Locate every blood parasite and identify its species.
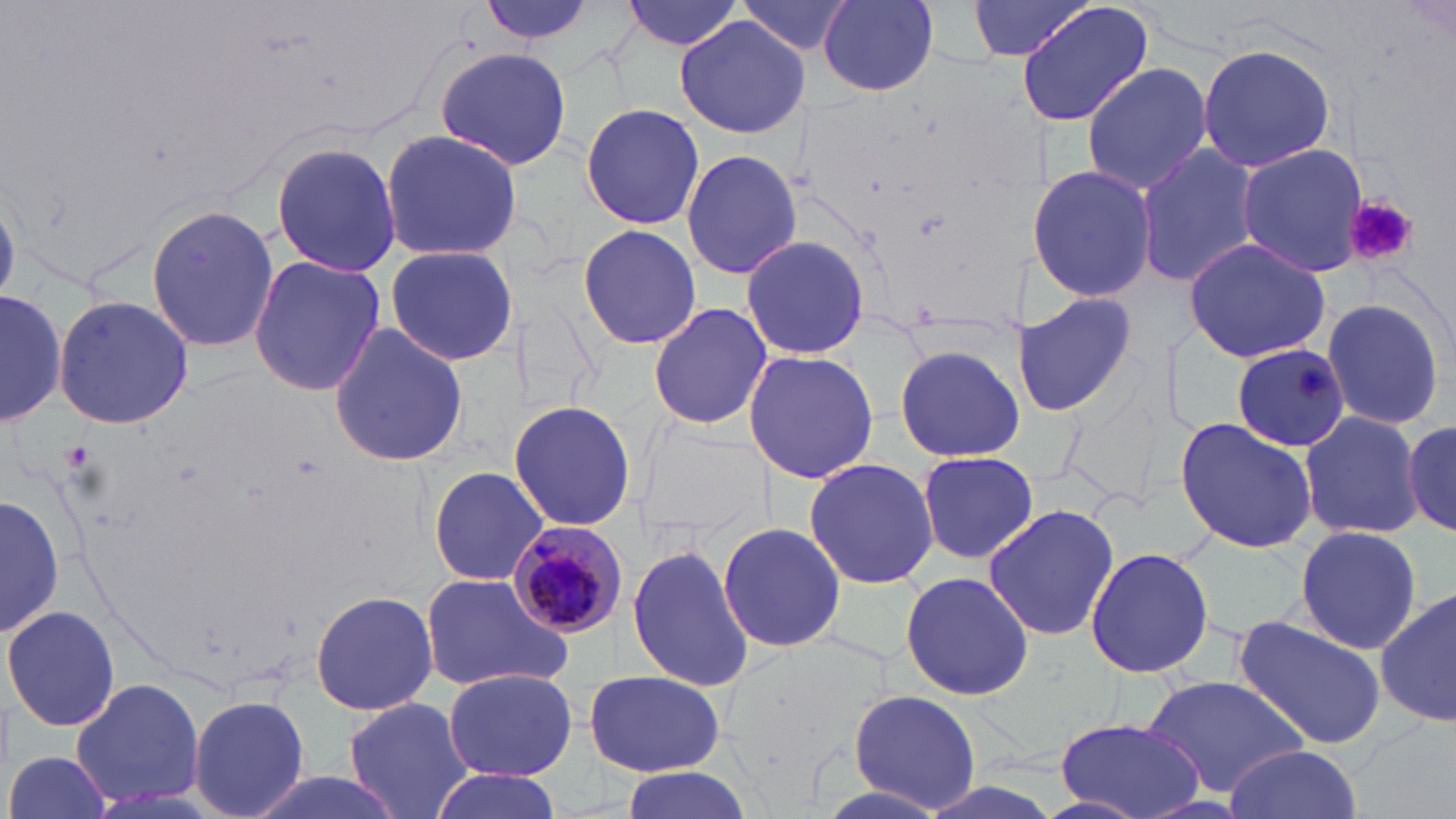

Approximate bounding boxes as (x1,y1)-(x2,y2) corner pairs in pixels.
Plasmodium malariae-infected red blood cells: (508,520)-(628,640).
No Plasmodium falciparum, Plasmodium ovale, Plasmodium vivax, Babesia divergens, or Trypanosoma brucei observed.

Summary:
  - Uninfected red blood cell locations: (469,0)-(608,51), (618,0)-(746,54), (818,0)-(939,94), (967,0)-(1090,60), (738,1)-(851,53), (1015,1)-(1154,128), (673,14)-(809,137), (1196,42)-(1335,173), (435,47)-(572,172), (1080,61)-(1213,195), (581,101)-(705,230), (378,128)-(522,260), (269,139)-(404,279), (1136,141)-(1260,288), (1236,143)-(1369,278), (680,148)-(802,281), (1029,163)-(1158,302), (146,201)-(279,353), (577,223)-(701,352), (742,236)-(871,358), (1183,237)-(1331,363), (385,245)-(518,365), (247,255)-(385,397), (1018,288)-(1143,418), (2,289)-(64,426), (53,295)-(193,430), (1320,297)-(1448,430), (647,302)-(773,432), (329,321)-(469,469), (893,342)-(1024,462), (1231,342)-(1352,451), (742,350)-(879,484), (508,398)-(635,532), (1298,410)-(1425,539), (1176,416)-(1319,554), (1404,420)-(1456,536), (917,450)-(1037,564), (803,461)-(939,587), (427,465)-(550,586), (1,494)-(63,637), (983,500)-(1120,644), (717,521)-(846,652), (1294,526)-(1423,652), (627,542)-(755,692), (1084,546)-(1217,681), (899,568)-(1036,701), (418,571)-(574,692), (1375,588)-(1456,728), (309,589)-(439,717), (3,605)-(120,733), (1233,614)-(1388,753), (441,667)-(578,781), (584,668)-(727,778), (1139,674)-(1310,797), (69,677)-(205,809), (845,690)-(984,812), (188,694)-(310,819), (343,697)-(475,819), (1055,714)-(1206,818), (1223,745)-(1361,818), (6,750)-(112,819), (613,765)-(756,819), (428,767)-(562,819), (238,770)-(413,819)
  - Platelet locations: (1345,196)-(1419,267), (1295,366)-(1335,400)
  - Slide-level diagnosis: Plasmodium malariae
  - Preparation: thin blood film
  - Image size: 1456×819 pixels
  - Stain: May-Grünwald-Giemsa
  - Magnification: 1000x
  - Field of view: one of a larger specimen
  - Modality: light microscopy